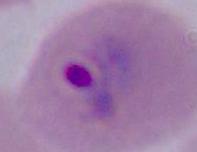

Photomicrograph. 400x or 1000x magnification. A Plasmodium parasite is seen.